Locate leukocytes (white blood cells).
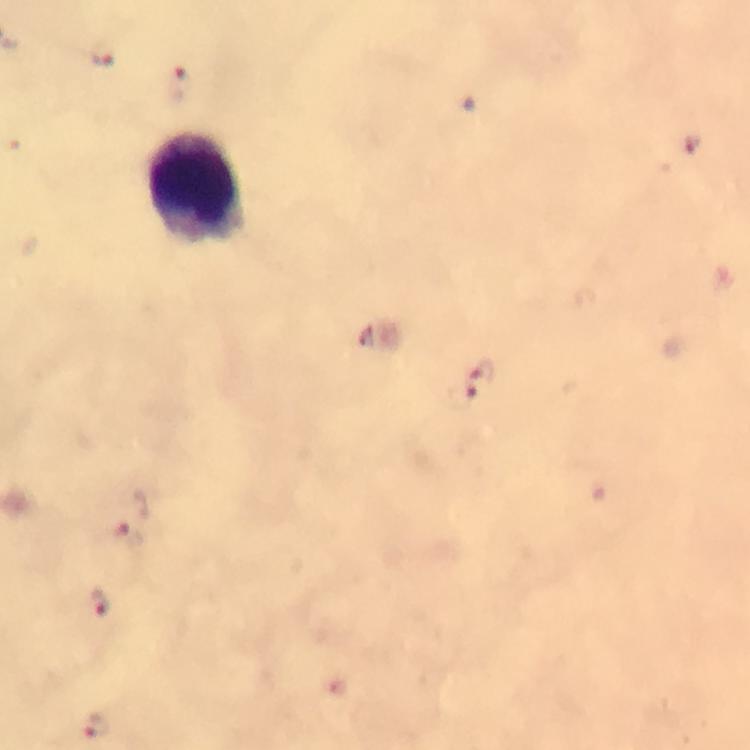

Approximate object centers, in pixels from the top-left corner.
Leukocytes: (x=200, y=188).

Malaria parasite locations: (x=102, y=58), (x=176, y=85), (x=691, y=145), (x=480, y=383), (x=124, y=536), (x=103, y=603), (x=97, y=728). 100x magnification. Photographed through the microscope with a smartphone camera. Thick blood film. Immersion oil was used. A crop from one field of view. From a diagnostic examination for malaria. Giemsa stain. Image is 750×750 pixels.